Point out leukocytes.
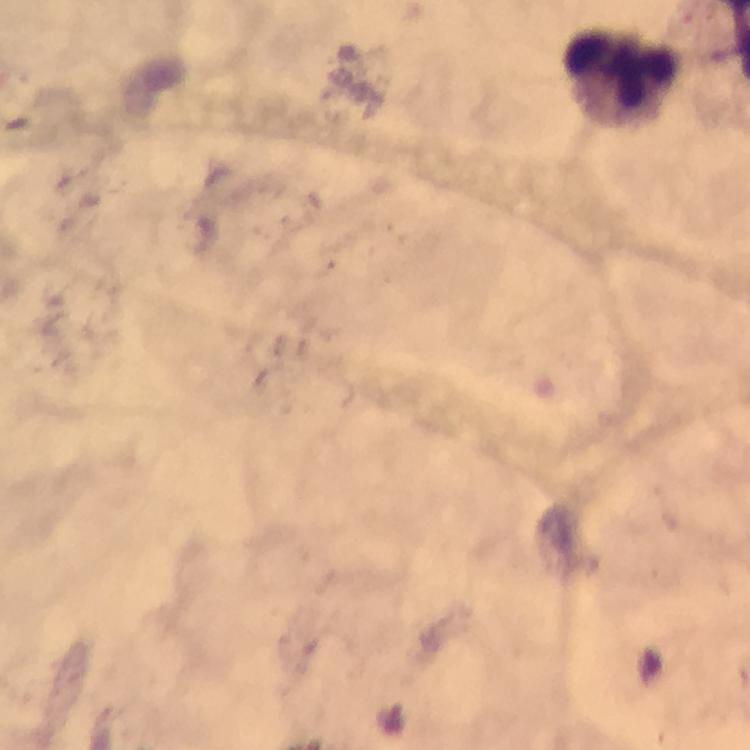

Approximate object centers, in pixels from the top-left corner.
Leukocytes: (x=624, y=76).

Thick blood film. Photographed through the microscope with a smartphone camera. Cropped region of a single field of view. At 100x magnification. Giemsa-stained preparation. Image is 750×750 pixels. Immersion oil was used. From a malaria diagnostic workup. Plasmodium parasites: none detected.